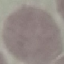

malaria status = uninfected
preparation = thin blood film
image type = cell patch, automatically extracted from a larger field of view and resized to 64 × 64 pixels
stain = Giemsa
capture = smartphone through the microscope eyepiece